Name the parasite shown.
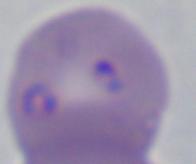

This is Babesia.

Micrograph. 1000x magnification.